Locate every blood parasite and identify its species.
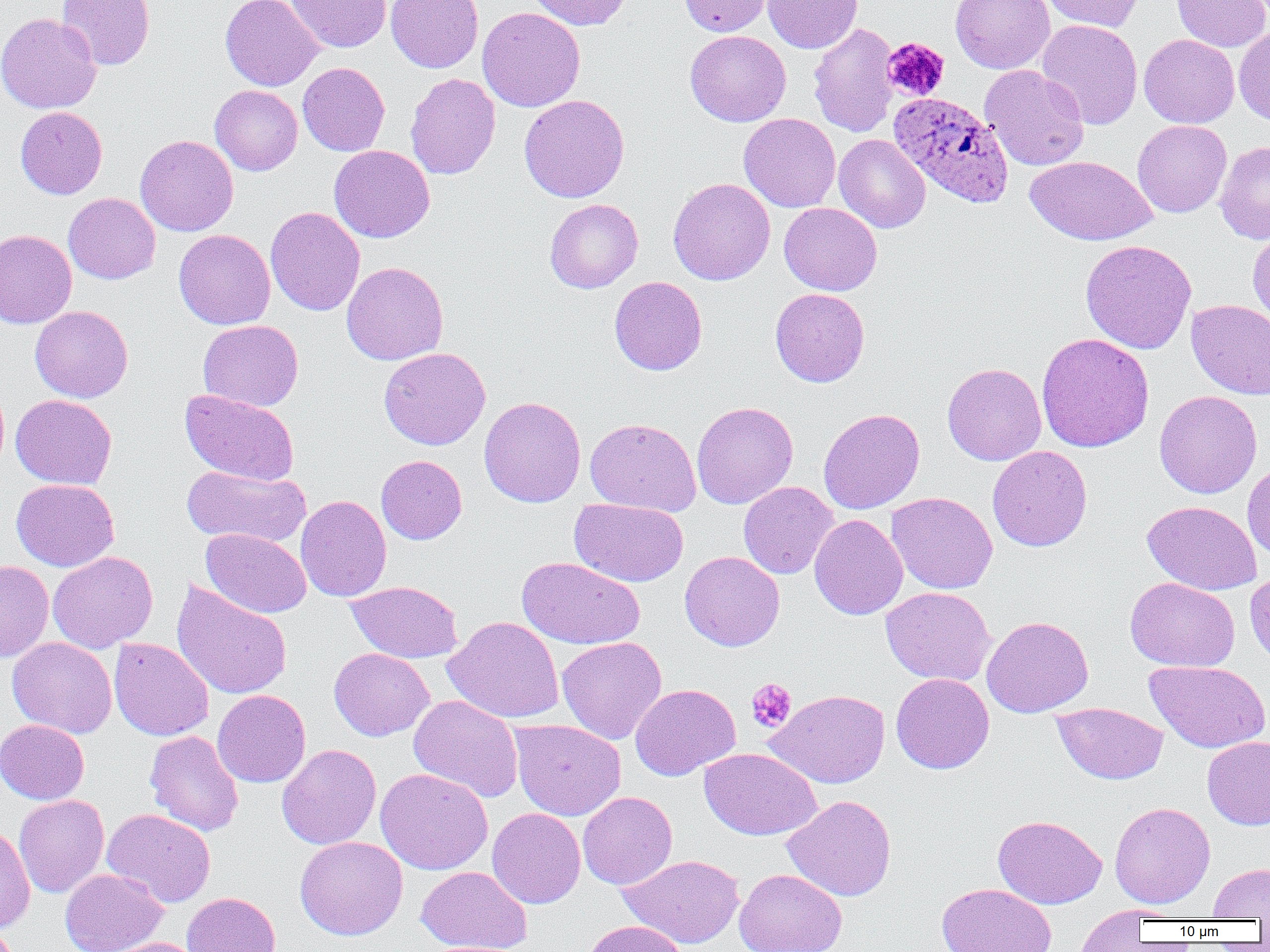
Approximate bounding boxes as named x1/y1/x2/y2 corners in pixels.
Plasmodium ovale-infected red blood cells: (x1=888, y1=91, x2=1014, y2=207).
No Plasmodium falciparum, Plasmodium malariae, Plasmodium vivax, Babesia divergens, or Trypanosoma brucei observed.

slide-level diagnosis = Plasmodium ovale
uninfected red blood cell locations = approximate bounding boxes as named x1/y1/x2/y2 corners in pixels: (x1=56, y1=0, x2=155, y2=70), (x1=220, y1=0, x2=324, y2=91), (x1=286, y1=0, x2=391, y2=53), (x1=385, y1=0, x2=483, y2=73), (x1=526, y1=0, x2=632, y2=30), (x1=679, y1=0, x2=773, y2=36), (x1=763, y1=0, x2=862, y2=53), (x1=950, y1=0, x2=1055, y2=74), (x1=1042, y1=0, x2=1143, y2=32), (x1=1171, y1=0, x2=1270, y2=52), (x1=477, y1=7, x2=585, y2=112), (x1=0, y1=13, x2=102, y2=113), (x1=1036, y1=19, x2=1143, y2=130), (x1=808, y1=22, x2=900, y2=137), (x1=1234, y1=27, x2=1270, y2=125), (x1=685, y1=30, x2=790, y2=126), (x1=1139, y1=34, x2=1239, y2=128), (x1=298, y1=62, x2=390, y2=156), (x1=980, y1=65, x2=1089, y2=171), (x1=405, y1=73, x2=501, y2=180), (x1=209, y1=85, x2=303, y2=175), (x1=519, y1=94, x2=630, y2=203), (x1=15, y1=106, x2=107, y2=199), (x1=738, y1=113, x2=840, y2=212), (x1=1132, y1=120, x2=1232, y2=217), (x1=834, y1=134, x2=931, y2=233), (x1=135, y1=135, x2=239, y2=236), (x1=1215, y1=140, x2=1270, y2=244), (x1=329, y1=145, x2=435, y2=243), (x1=1025, y1=155, x2=1157, y2=246), (x1=668, y1=177, x2=775, y2=285), (x1=63, y1=192, x2=160, y2=283), (x1=544, y1=199, x2=644, y2=293), (x1=779, y1=202, x2=882, y2=295), (x1=265, y1=206, x2=365, y2=316), (x1=1247, y1=226, x2=1270, y2=328), (x1=0, y1=229, x2=77, y2=329), (x1=173, y1=229, x2=275, y2=330), (x1=1081, y1=239, x2=1197, y2=354), (x1=341, y1=262, x2=449, y2=365), (x1=609, y1=276, x2=707, y2=375), (x1=770, y1=288, x2=870, y2=387), (x1=1186, y1=300, x2=1270, y2=399), (x1=30, y1=305, x2=133, y2=402), (x1=198, y1=320, x2=304, y2=411), (x1=1036, y1=333, x2=1155, y2=453), (x1=378, y1=347, x2=491, y2=450), (x1=942, y1=362, x2=1046, y2=465), (x1=180, y1=390, x2=300, y2=485), (x1=1154, y1=390, x2=1262, y2=498), (x1=10, y1=394, x2=117, y2=489), (x1=479, y1=396, x2=586, y2=507), (x1=692, y1=401, x2=798, y2=509), (x1=818, y1=408, x2=925, y2=514), (x1=585, y1=418, x2=701, y2=516), (x1=987, y1=446, x2=1092, y2=552), (x1=376, y1=455, x2=467, y2=545), (x1=1242, y1=461, x2=1270, y2=563), (x1=182, y1=464, x2=310, y2=548), (x1=11, y1=479, x2=119, y2=571), (x1=738, y1=481, x2=838, y2=579), (x1=885, y1=492, x2=998, y2=594), (x1=295, y1=495, x2=391, y2=602), (x1=569, y1=498, x2=689, y2=587), (x1=1142, y1=501, x2=1262, y2=595), (x1=809, y1=514, x2=908, y2=620), (x1=201, y1=528, x2=311, y2=618), (x1=47, y1=551, x2=158, y2=653), (x1=680, y1=551, x2=785, y2=651), (x1=517, y1=557, x2=646, y2=650), (x1=0, y1=560, x2=53, y2=662), (x1=1245, y1=568, x2=1270, y2=667), (x1=1125, y1=577, x2=1240, y2=672), (x1=171, y1=579, x2=293, y2=701), (x1=345, y1=581, x2=463, y2=663), (x1=881, y1=586, x2=996, y2=686), (x1=443, y1=615, x2=564, y2=723), (x1=981, y1=616, x2=1093, y2=717), (x1=8, y1=637, x2=117, y2=738), (x1=109, y1=637, x2=214, y2=741), (x1=557, y1=637, x2=667, y2=744), (x1=329, y1=647, x2=434, y2=741), (x1=1145, y1=660, x2=1270, y2=753), (x1=891, y1=673, x2=995, y2=774), (x1=630, y1=683, x2=740, y2=780), (x1=212, y1=690, x2=311, y2=788), (x1=767, y1=690, x2=890, y2=788), (x1=409, y1=694, x2=524, y2=802), (x1=1052, y1=702, x2=1168, y2=785), (x1=0, y1=719, x2=89, y2=804), (x1=510, y1=719, x2=626, y2=820), (x1=144, y1=730, x2=244, y2=836), (x1=1202, y1=736, x2=1270, y2=830), (x1=276, y1=743, x2=381, y2=849), (x1=699, y1=748, x2=822, y2=840), (x1=375, y1=767, x2=493, y2=875), (x1=578, y1=791, x2=677, y2=889), (x1=14, y1=794, x2=110, y2=898), (x1=782, y1=795, x2=897, y2=902), (x1=1109, y1=801, x2=1215, y2=909), (x1=102, y1=808, x2=216, y2=908), (x1=487, y1=808, x2=586, y2=908), (x1=993, y1=814, x2=1107, y2=908), (x1=0, y1=824, x2=35, y2=935), (x1=295, y1=835, x2=408, y2=940), (x1=618, y1=854, x2=744, y2=948), (x1=1208, y1=862, x2=1270, y2=920), (x1=416, y1=866, x2=532, y2=952), (x1=59, y1=868, x2=168, y2=952), (x1=734, y1=869, x2=847, y2=952), (x1=936, y1=882, x2=1057, y2=952), (x1=182, y1=892, x2=281, y2=952), (x1=1074, y1=907, x2=1151, y2=951), (x1=582, y1=919, x2=690, y2=952), (x1=99, y1=937, x2=204, y2=952)
image size = 1270×952 pixels
modality = light microscopy
platelet locations = approximate bounding boxes as named x1/y1/x2/y2 corners in pixels: (x1=882, y1=37, x2=950, y2=101), (x1=745, y1=678, x2=797, y2=732)
field of view = single
magnification = 1000x
preparation = thin blood smear